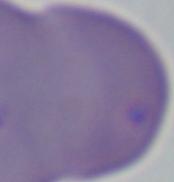

Micrograph. 1000x magnification. A Babesia parasite is shown.